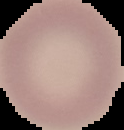
Summary:
  - Image type: segmented cell region on a black background
  - Malaria status: uninfected
  - Image size: 124×130 pixels
  - Preparation: thin blood smear